Report the malaria status of this cell.
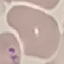
It is parasitized.

preparation: thin smear
image_type: cell patch, automatically extracted from a larger field of view and resized to 64 × 64 pixels
stain: Giemsa
capture: smartphone camera at the microscope eyepiece